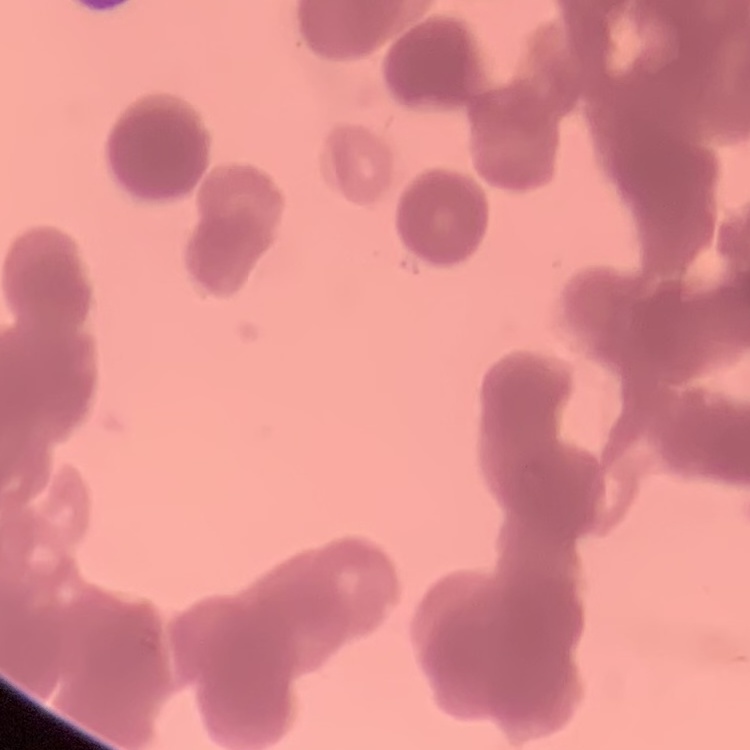
Summary:
  - Erythrocyte morphology: rouleaux formation
  - Image type: square crop of a larger photomicrograph
  - Preparation: thin blood smear
  - Stain: Field's or Giemsa